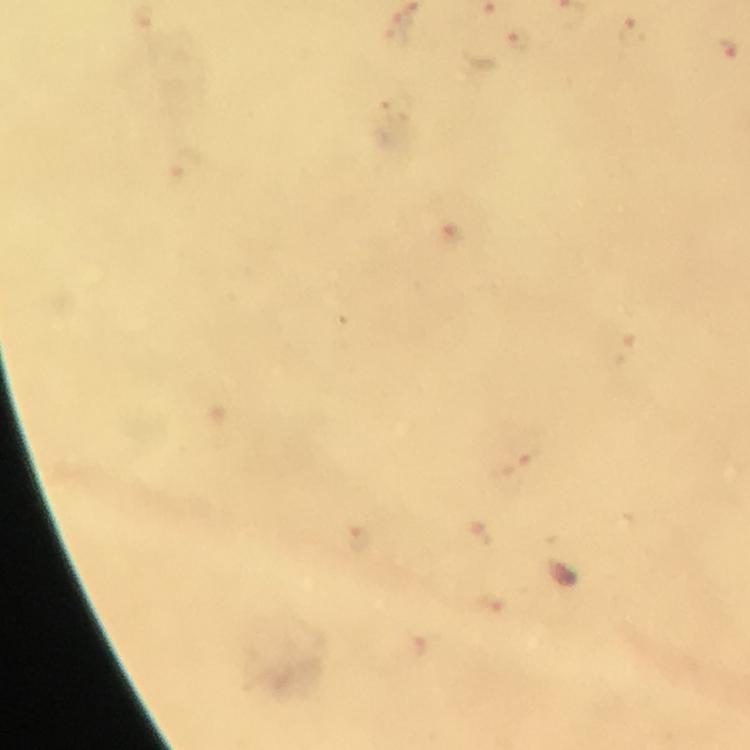

Approximate centers as (x, y) in pixels.
Summary:
  - Malaria parasite locations: (404, 27), (634, 32), (517, 43), (724, 51), (526, 452), (480, 532), (361, 539)
  - Context: from a malaria diagnostic workup
  - Cropped from: a single field of view
  - Preparation: thick blood film
  - Image size: 750×750 pixels
  - Magnification: 100x
  - Capture: smartphone photograph through a microscope
  - Immersion oil: used
  - Stain: Giemsa